Identify the preparation type.
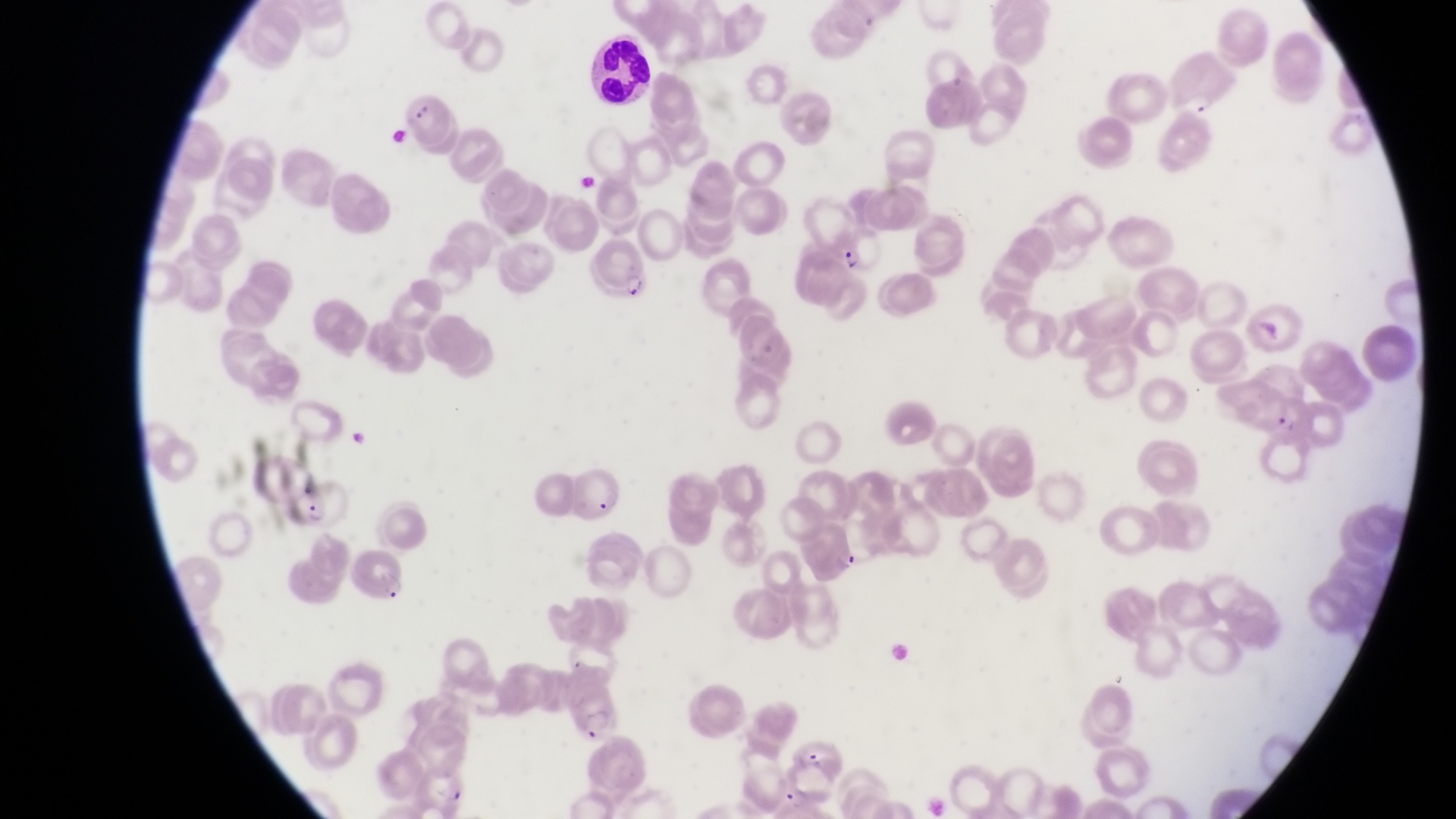
Thin blood film.

Approximate bounding boxes as left top right bottom in pixels.
Summary:
  - Parasitised red blood cell locations: 1172 55 1236 116; 399 95 446 147; 825 224 880 273; 587 240 650 301; 1263 393 1319 448; 278 479 349 532; 792 521 861 582; 346 548 412 611; 561 680 621 741; 788 737 844 782; 415 766 471 815
  - Leukocyte locations: 578 40 652 109
  - Country: Uganda
  - Capture: smartphone photograph through the eyepiece of an Olympus CX-23 microscope
  - Image size: 1456×819 pixels
  - Magnification: 1000x
  - Field of view: single